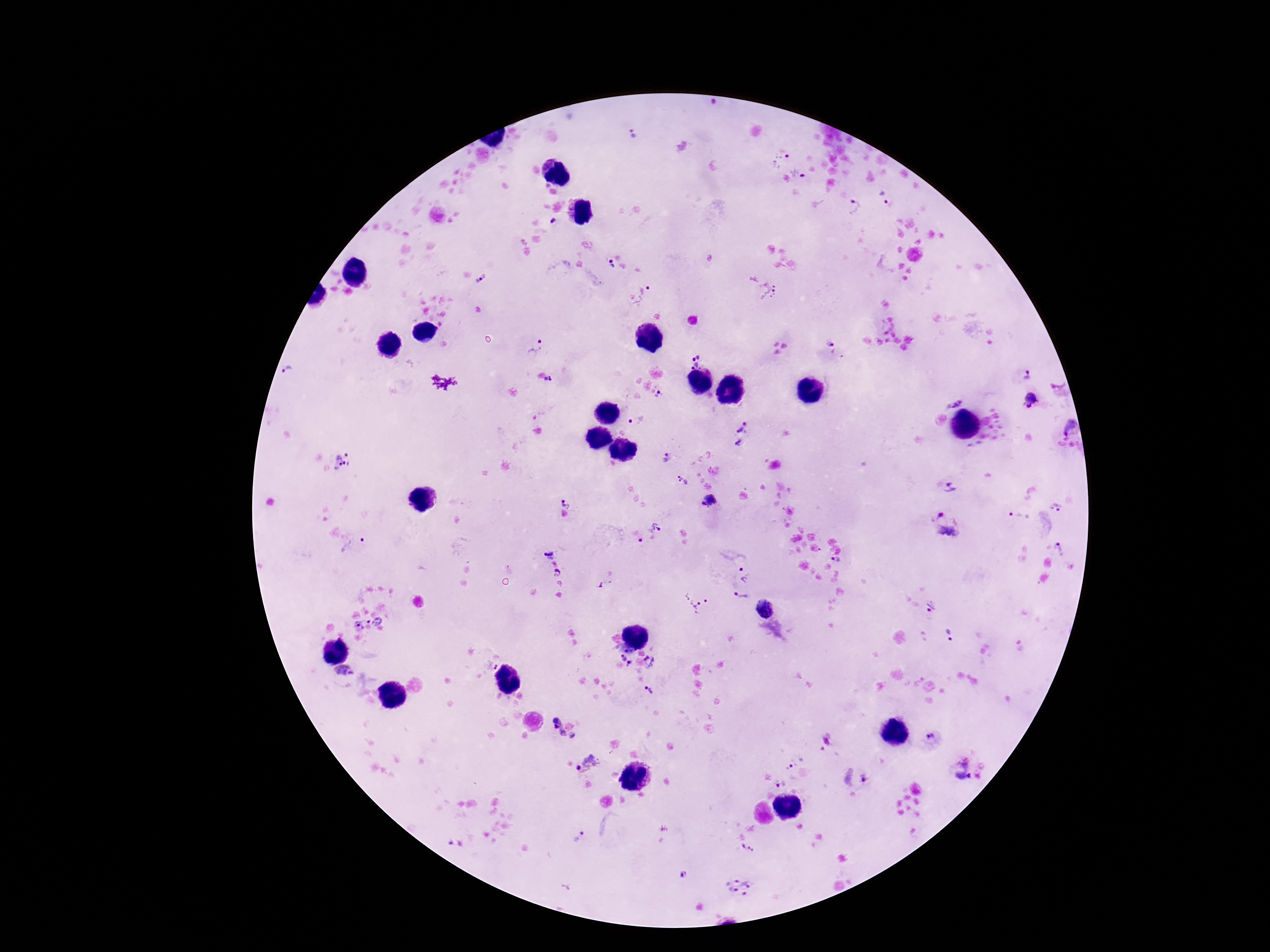

Approximate centers as (x, y) in pixels. Plasmodium parasite locations: (632, 135), (783, 162), (797, 174), (882, 194), (853, 207), (552, 221), (608, 266), (481, 280), (646, 288), (770, 289), (830, 344), (535, 349), (694, 360), (1027, 375), (549, 380), (1059, 383), (660, 395), (952, 401), (1032, 402), (637, 421), (741, 425), (1070, 428), (739, 443), (665, 455), (343, 463), (681, 482), (953, 487), (709, 501), (566, 502), (1057, 507), (940, 513), (1018, 517), (948, 529), (656, 531), (640, 541), (1060, 549), (353, 550), (547, 553), (837, 559), (558, 573), (745, 574), (560, 583), (558, 595), (741, 597), (696, 602), (931, 608), (765, 609), (378, 621), (369, 622), (360, 626), (948, 635), (626, 659), (649, 663), (492, 666), (346, 672), (649, 689), (564, 728), (932, 738), (793, 760), (587, 764), (962, 770), (855, 776), (781, 782), (579, 838), (455, 844), (748, 850), (684, 875), (738, 886). Image is 1270×952 pixels. Thick blood film. 100x magnification. Photographed through the microscope eyepiece with a smartphone camera. One field from this slide. Patient malaria status: infected. Giemsa stain.